Locate every Plasmodium falciparum-infected red blood cell.
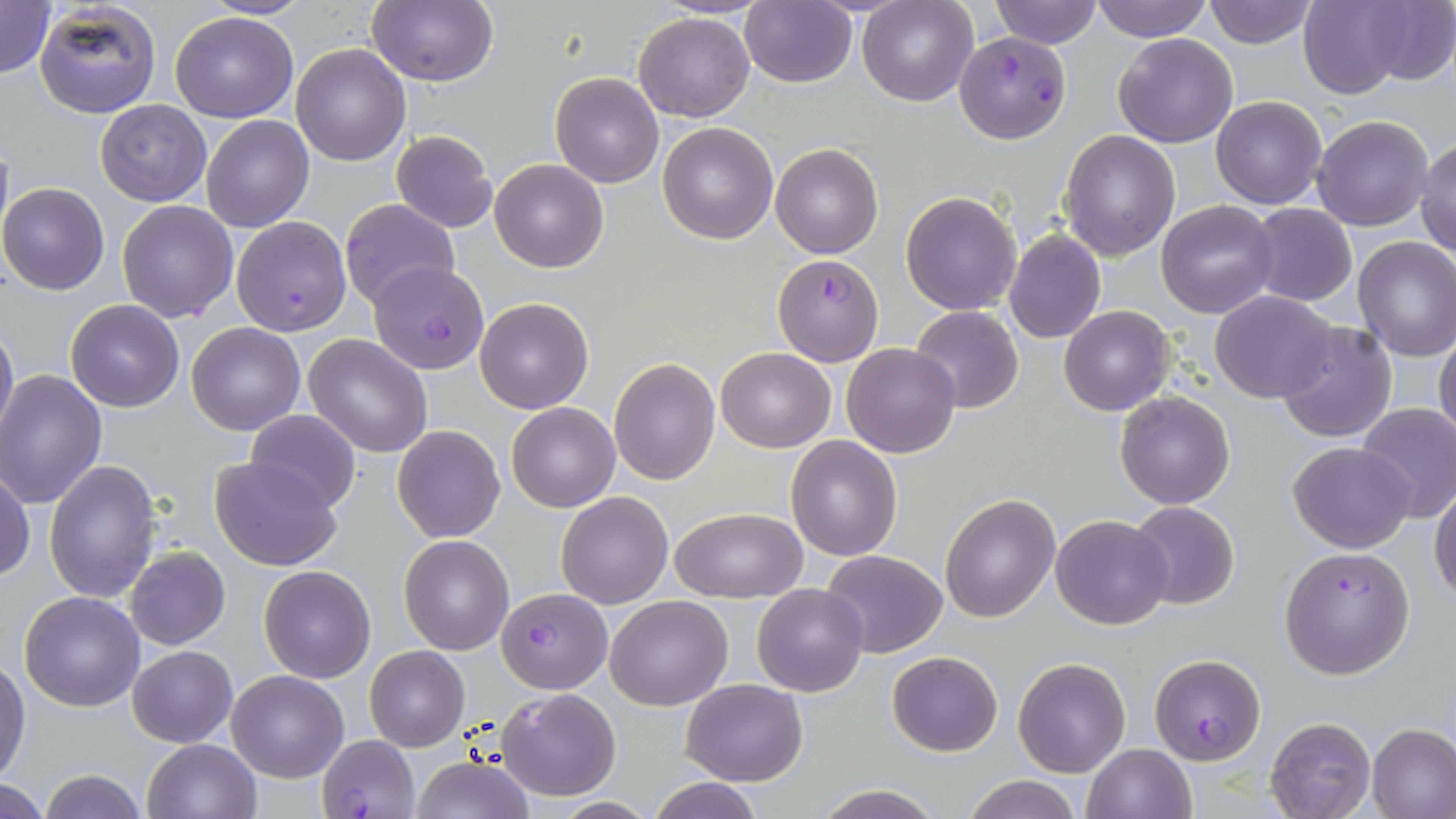

Approximate bounding boxes as (x1,y1)-(x2,y2) corner pairs in pixels.
Plasmodium falciparum-infected red blood cells: (954,31)-(1072,144), (231,215)-(352,337), (772,252)-(886,367), (368,261)-(491,375), (1279,546)-(1415,678), (497,587)-(610,691), (1150,653)-(1266,765), (317,735)-(420,818).

Uninfected red blood cell locations: (0,0)-(55,79), (33,0)-(161,118), (201,0)-(312,20), (367,0)-(496,86), (655,0)-(771,19), (738,0)-(858,87), (859,0)-(977,105), (988,0)-(1103,48), (1092,0)-(1212,40), (1201,0)-(1318,49), (1296,0)-(1420,98), (1358,0)-(1456,86), (170,11)-(298,123), (633,12)-(754,122), (1112,32)-(1238,148), (291,44)-(411,166), (550,72)-(664,188), (1210,95)-(1327,209), (95,100)-(212,205), (202,114)-(314,233), (1313,114)-(1435,232), (658,121)-(778,243), (391,129)-(498,232), (1061,130)-(1181,260), (0,136)-(14,250), (1416,139)-(1456,256), (771,142)-(884,259), (490,158)-(608,273), (0,182)-(111,294), (901,191)-(1021,314), (117,199)-(238,322), (338,199)-(459,310), (1156,201)-(1279,318), (1247,203)-(1357,307), (1004,230)-(1106,343), (1353,237)-(1456,361), (1210,292)-(1339,403), (475,296)-(595,414), (64,300)-(185,412), (1060,305)-(1175,415), (909,306)-(1025,413), (0,320)-(18,446), (1276,322)-(1398,443), (188,323)-(305,435), (1435,332)-(1456,446), (304,334)-(433,458), (840,342)-(961,458), (715,347)-(834,452), (609,358)-(719,484), (0,369)-(108,508), (1115,391)-(1235,510), (507,402)-(620,512), (1355,402)-(1456,521), (245,409)-(361,514), (392,425)-(506,543), (786,436)-(902,559), (1287,441)-(1416,553), (211,456)-(342,571), (45,459)-(162,604), (0,469)-(35,582), (1430,484)-(1456,602), (554,492)-(673,609), (941,494)-(1059,621), (1127,501)-(1239,609), (669,507)-(807,601), (1051,513)-(1173,630), (400,535)-(513,655), (124,546)-(231,650), (820,549)-(948,659), (260,565)-(377,683), (752,583)-(869,697), (19,591)-(146,711), (605,595)-(730,710), (127,646)-(237,747), (364,647)-(469,751), (886,650)-(1004,757), (1013,657)-(1130,777), (0,659)-(29,781), (228,670)-(347,781), (682,678)-(807,785), (497,686)-(620,800), (1266,716)-(1376,819), (1368,723)-(1456,818), (143,738)-(262,819), (1082,743)-(1197,819), (411,755)-(537,819), (38,769)-(148,819), (960,776)-(1084,819), (646,777)-(766,818), (0,782)-(52,819), (811,783)-(944,818). Slide-level diagnosis: Plasmodium falciparum. 1000x magnification. May-Grünwald-Giemsa stain. Light microscopy. Image is 1456×819 pixels. Single field of view. Thin blood smear.